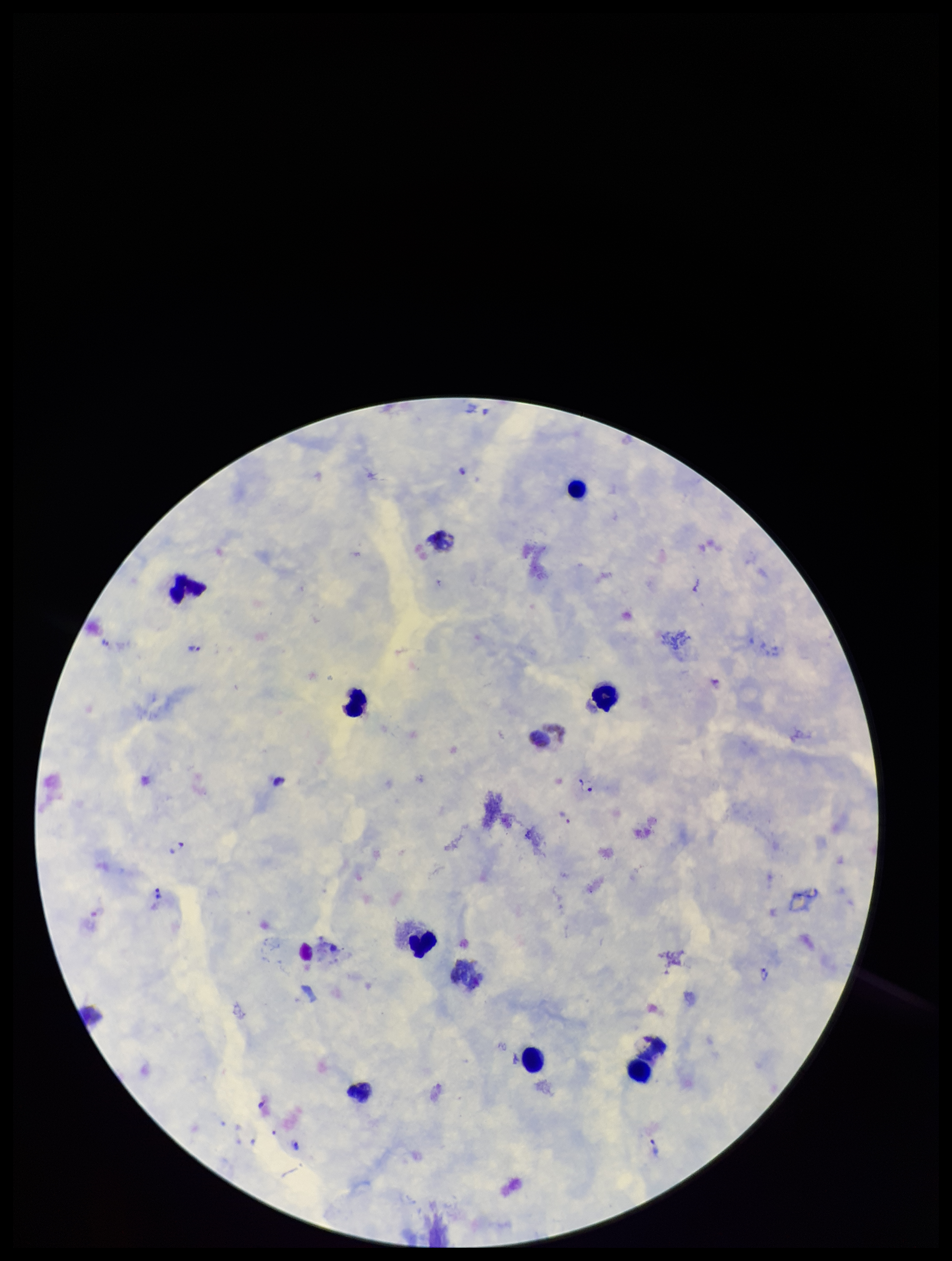

patient malaria status = positive
parasite count = 7
preparation = thick smear
stain = Giemsa
Plasmodium parasites = identified
species reported for this patient = Plasmodium vivax
image size = 952×1261 pixels
field of view = single
leukocyte count = 9
capture = smartphone photograph through the microscope eyepiece